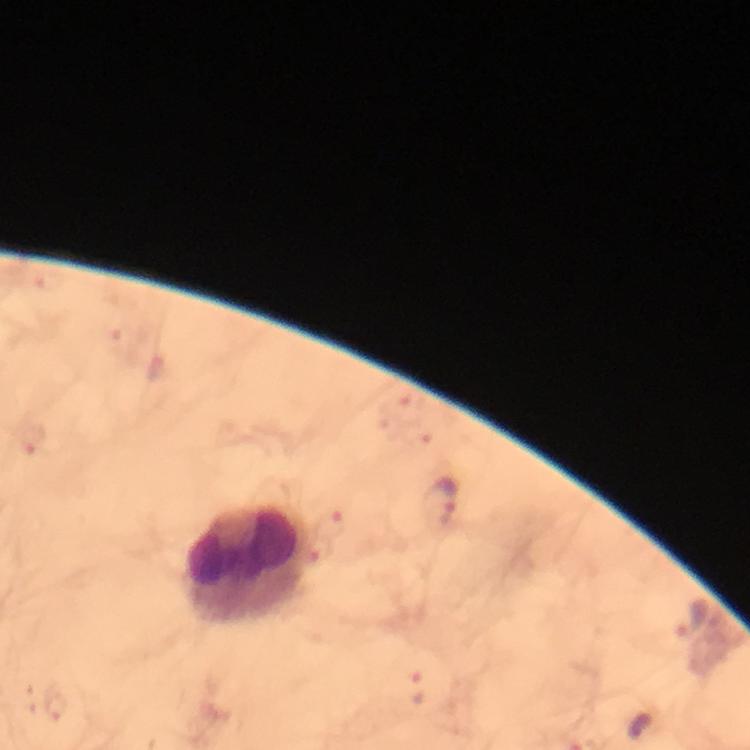 Approximate object centers, in pixels from the top-left corner. Malaria parasite locations: (x=34, y=440), (x=440, y=504), (x=689, y=618), (x=417, y=690), (x=53, y=704). Leukocyte locations: (x=250, y=561). Immersion oil was used. A crop from one field of view. Giemsa-stained preparation. Photographed with a smartphone mounted on the microscope. From a diagnostic examination for malaria. Image is 750×750 pixels. Thick blood film. At 100x magnification.